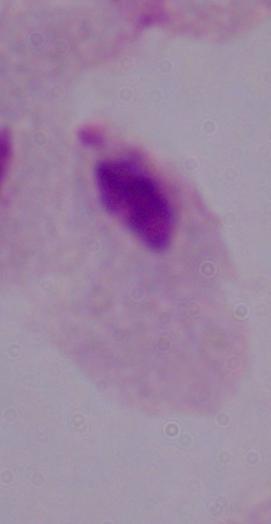
A trichomonad is shown. 1000x magnification. Micrograph.